Describe the morphology of the erythrocytes.
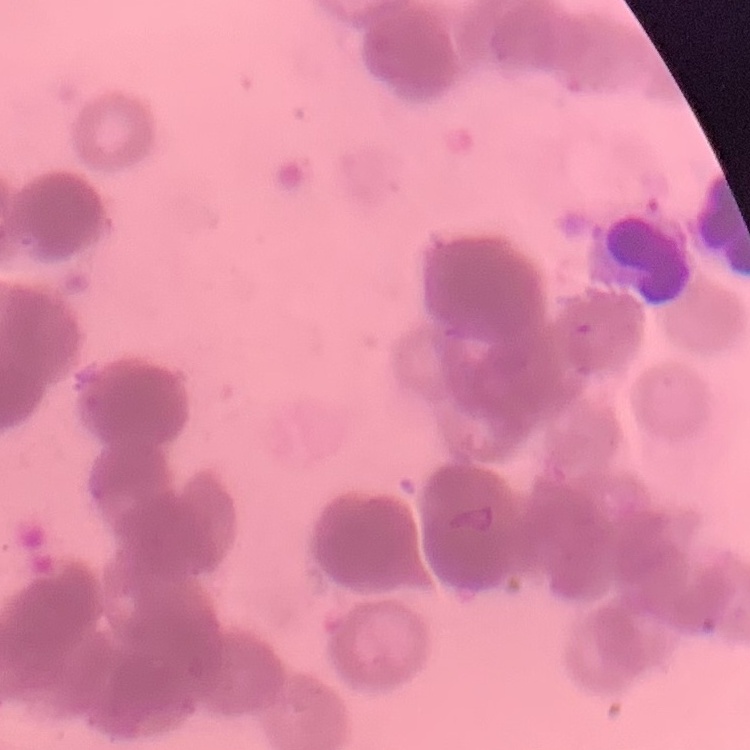
They show rouleaux formation.

stain: Field's or Giemsa
preparation: thin peripheral smear
image_type: one tile cut from a larger photomicrograph